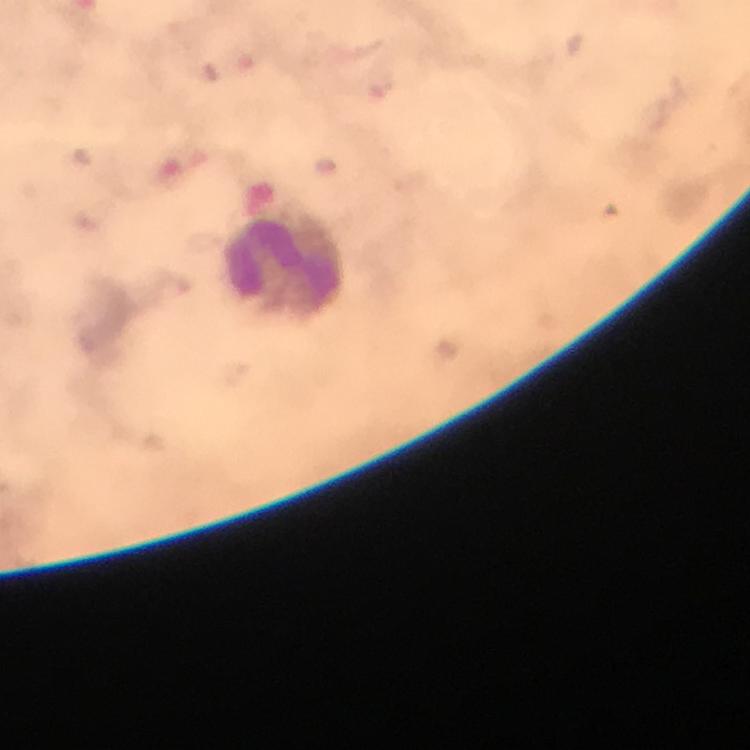
stain = Giemsa
leukocyte locations = approximate centers as [x, y] in pixels: [286, 264]
context = from a diagnostic examination for malaria
cropped from = one field of view
capture = smartphone photograph through a microscope
image size = 750×750 pixels
immersion oil = used
preparation = thick blood film
malaria parasites = none seen
magnification = 100x